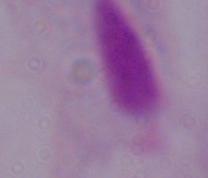

modality: micrograph
identification: trichomonad
magnification: 1000x